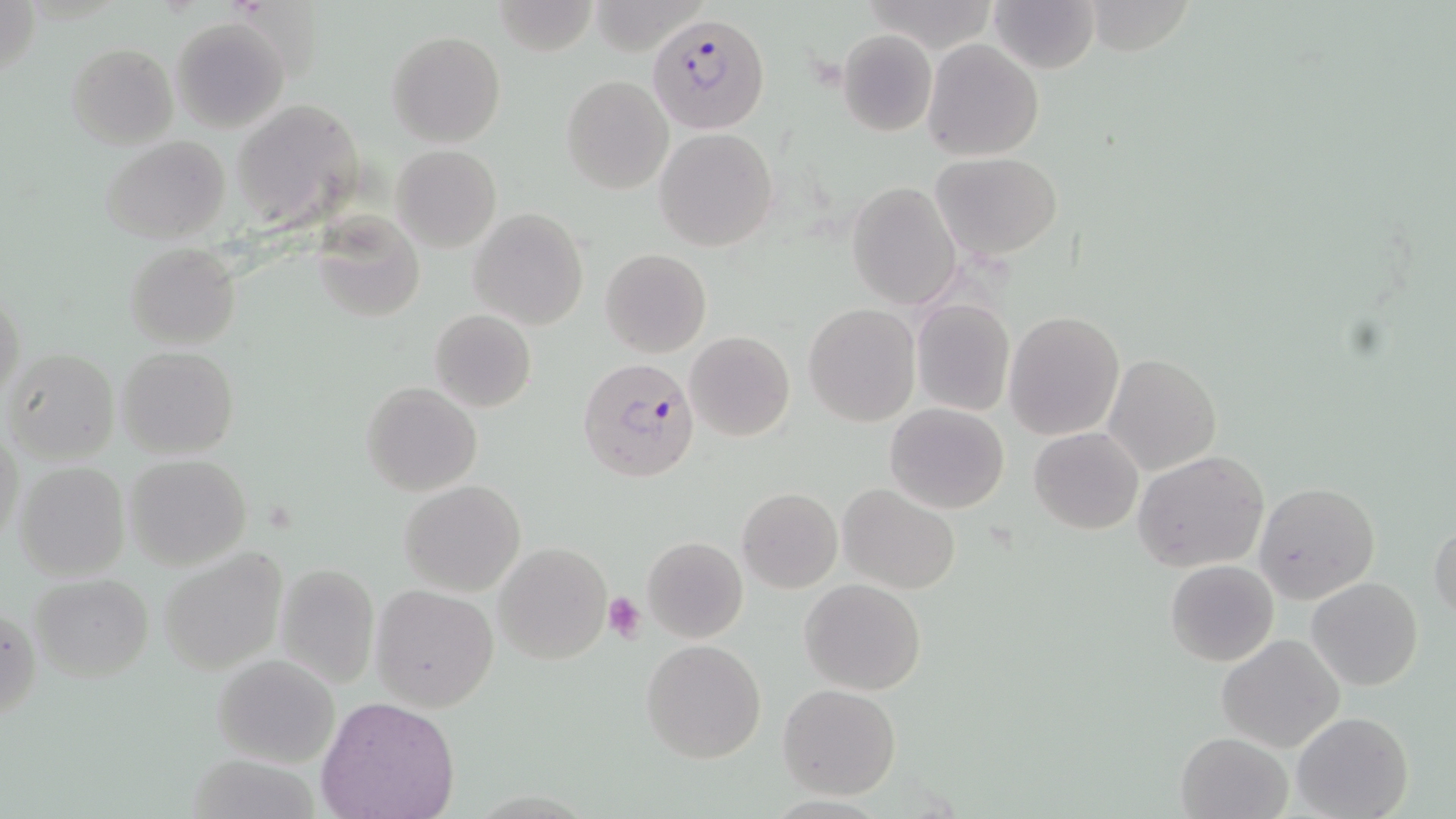
slide_level_diagnosis: Plasmodium falciparum
image_size: 1456×819 pixels
field_of_view: single
modality: light microscopy
magnification: 1000x
plasmodium_falciparum_infected_red_blood_cell_locations: 'approximate bounding boxes as named x1/y1/x2/y2 corners in pixels: (x1=643, y1=15, x2=766, y2=133), (x1=577, y1=357, x2=700, y2=484)'
uninfected_red_blood_cell_locations: 'approximate bounding boxes as named x1/y1/x2/y2 corners in pixels: (x1=1, y1=0, x2=41, y2=89), (x1=491, y1=0, x2=597, y2=55), (x1=987, y1=0, x2=1100, y2=74), (x1=171, y1=17, x2=289, y2=131), (x1=836, y1=30, x2=938, y2=136), (x1=387, y1=31, x2=505, y2=147), (x1=921, y1=39, x2=1043, y2=162), (x1=66, y1=42, x2=177, y2=149), (x1=560, y1=75, x2=674, y2=194), (x1=231, y1=101, x2=367, y2=230), (x1=655, y1=128, x2=778, y2=252), (x1=100, y1=136, x2=231, y2=244), (x1=392, y1=144, x2=501, y2=252), (x1=930, y1=152, x2=1062, y2=261), (x1=846, y1=182, x2=962, y2=310), (x1=469, y1=209, x2=588, y2=330), (x1=313, y1=215, x2=426, y2=323), (x1=124, y1=242, x2=242, y2=349), (x1=599, y1=248, x2=712, y2=357), (x1=0, y1=289, x2=24, y2=409), (x1=911, y1=299, x2=1015, y2=417), (x1=804, y1=303, x2=921, y2=426), (x1=430, y1=309, x2=537, y2=411), (x1=1004, y1=311, x2=1125, y2=441), (x1=686, y1=330, x2=794, y2=441), (x1=116, y1=345, x2=239, y2=460), (x1=5, y1=349, x2=118, y2=464), (x1=1103, y1=352, x2=1221, y2=475), (x1=361, y1=382, x2=483, y2=497), (x1=885, y1=403, x2=1010, y2=514), (x1=1, y1=426, x2=23, y2=551), (x1=1029, y1=427, x2=1143, y2=534), (x1=1133, y1=451, x2=1271, y2=574), (x1=125, y1=454, x2=251, y2=568), (x1=11, y1=461, x2=130, y2=580), (x1=399, y1=479, x2=526, y2=597), (x1=1255, y1=482, x2=1380, y2=603), (x1=838, y1=484, x2=961, y2=595), (x1=737, y1=488, x2=842, y2=593), (x1=1429, y1=516, x2=1456, y2=625), (x1=642, y1=536, x2=748, y2=642), (x1=494, y1=541, x2=614, y2=664), (x1=158, y1=550, x2=288, y2=673), (x1=1165, y1=559, x2=1280, y2=667), (x1=274, y1=561, x2=380, y2=688), (x1=29, y1=572, x2=155, y2=684), (x1=1307, y1=576, x2=1423, y2=691), (x1=800, y1=579, x2=926, y2=695), (x1=370, y1=585, x2=499, y2=711), (x1=1, y1=604, x2=42, y2=726), (x1=1217, y1=634, x2=1345, y2=752), (x1=639, y1=638, x2=767, y2=764), (x1=213, y1=655, x2=340, y2=767), (x1=777, y1=683, x2=901, y2=799), (x1=316, y1=696, x2=461, y2=819), (x1=1291, y1=710, x2=1414, y2=819), (x1=1175, y1=732, x2=1294, y2=819)'
platelet_locations: 'approximate bounding boxes as named x1/y1/x2/y2 corners in pixels: (x1=603, y1=593, x2=647, y2=643)'
stain: May-Grünwald-Giemsa
preparation: thin blood film